Point out each malaria parasite and each leukocyte.
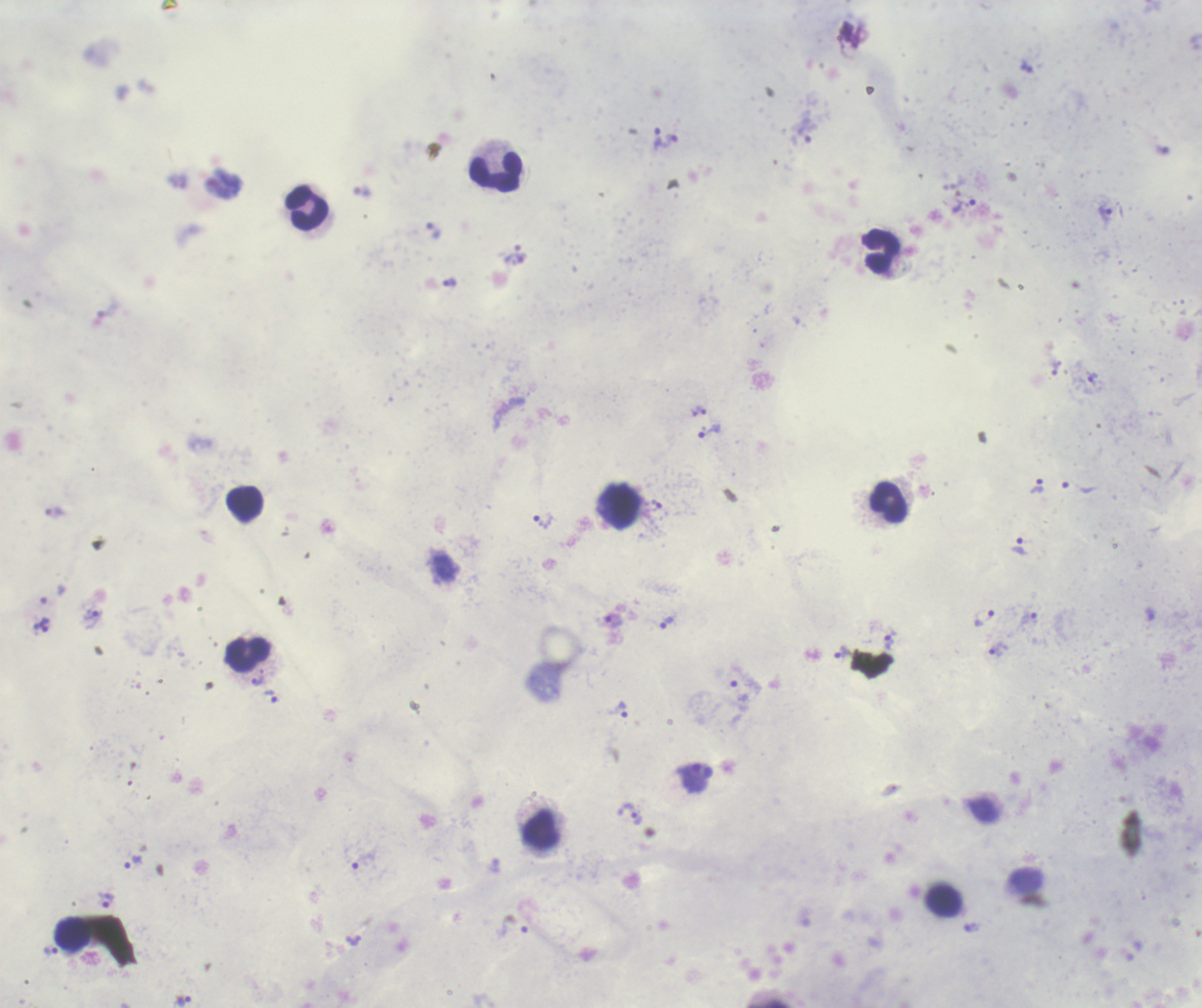
Approximate centers as {x, y} in pixels.
Trophozoites: {658, 138}, {671, 140}, {224, 183}, {964, 208}, {1106, 214}, {434, 231}, {514, 258}, {450, 283}, {1092, 378}, {701, 411}, {709, 432}, {1037, 486}, {656, 504}, {542, 522}, {1019, 545}, {983, 618}, {1029, 618}, {92, 620}, {614, 620}, {667, 622}, {41, 625}, {888, 643}, {997, 649}, {842, 652}, {258, 681}, {272, 697}, {623, 711}, {633, 816}, {133, 863}, {107, 900}, {356, 941}, {50, 951}, {184, 1001}.
No schizont or gametocyte forms observed.
Leukocytes: {496, 172}, {307, 208}, {880, 251}, {889, 502}, {244, 504}, {620, 507}, {248, 656}, {541, 829}, {943, 901}, {73, 932}.

Summary:
  - Background quality: good
  - Image size: 1202×1008 pixels
  - Field of view: one from this slide
  - Coloration quality: good
  - Stain: Romanowsky
  - Context: previously used in an actual diagnosis
  - Preparation: thick blood smear
  - Magnification: 100x